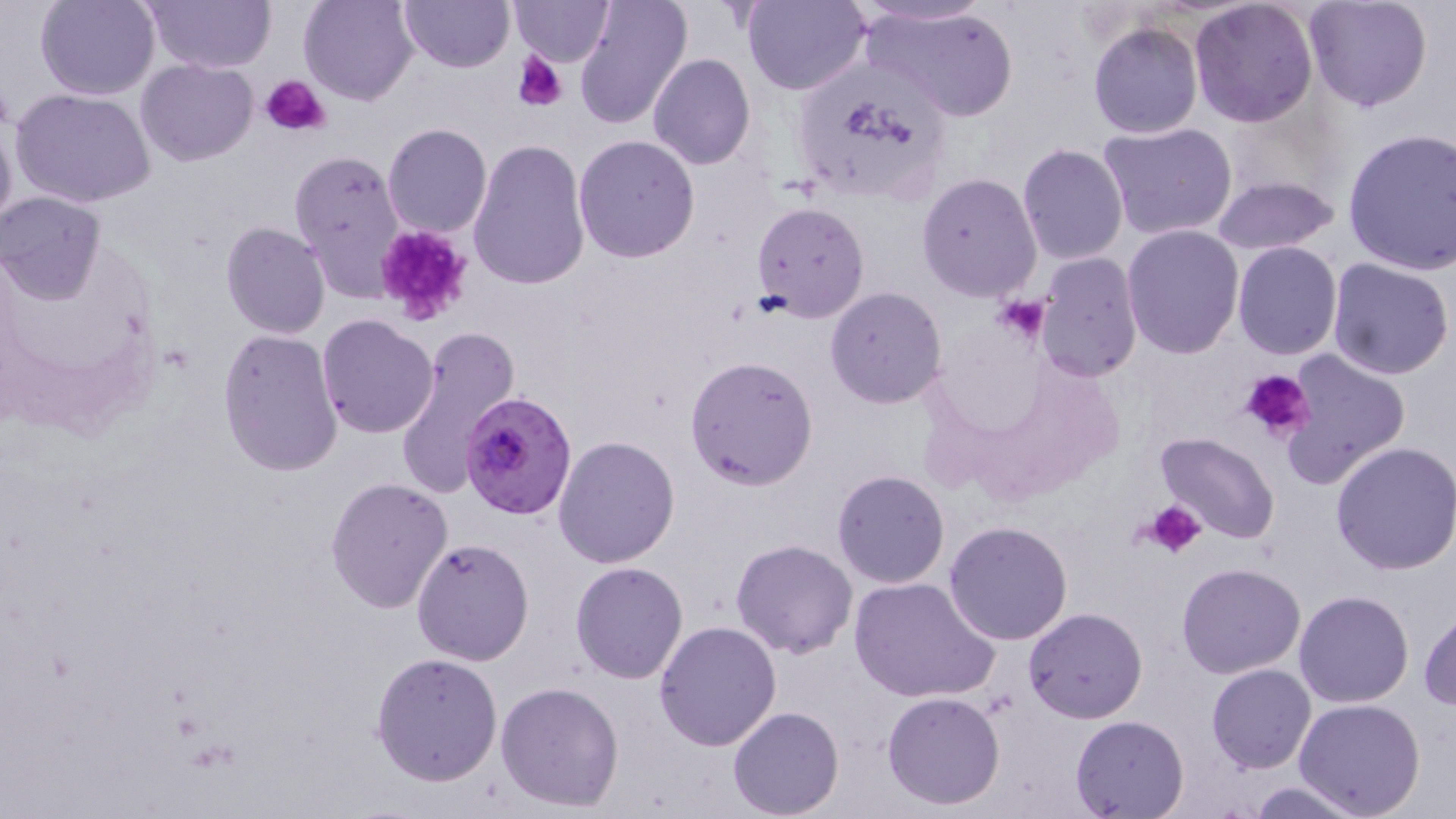 Approximate bounding boxes as named x1/y1/x2/y2 corners in pixels. Uninfected red blood cell locations: (x1=35, y1=0, x2=160, y2=100), (x1=140, y1=0, x2=277, y2=74), (x1=298, y1=0, x2=419, y2=107), (x1=397, y1=0, x2=513, y2=71), (x1=508, y1=0, x2=613, y2=65), (x1=574, y1=0, x2=693, y2=129), (x1=741, y1=0, x2=870, y2=95), (x1=849, y1=0, x2=998, y2=29), (x1=1190, y1=0, x2=1320, y2=128), (x1=1304, y1=0, x2=1434, y2=113), (x1=862, y1=5, x2=1019, y2=122), (x1=1088, y1=22, x2=1202, y2=139), (x1=648, y1=54, x2=756, y2=169), (x1=136, y1=59, x2=257, y2=167), (x1=12, y1=89, x2=155, y2=208), (x1=0, y1=98, x2=18, y2=243), (x1=1098, y1=122, x2=1240, y2=242), (x1=383, y1=123, x2=493, y2=239), (x1=1338, y1=127, x2=1456, y2=275), (x1=573, y1=134, x2=701, y2=263), (x1=468, y1=138, x2=591, y2=293), (x1=1017, y1=142, x2=1129, y2=266), (x1=287, y1=147, x2=408, y2=297), (x1=916, y1=172, x2=1041, y2=303), (x1=1210, y1=177, x2=1341, y2=256), (x1=0, y1=191, x2=107, y2=303), (x1=750, y1=201, x2=870, y2=321), (x1=220, y1=220, x2=332, y2=340), (x1=1121, y1=224, x2=1246, y2=359), (x1=1230, y1=241, x2=1342, y2=361), (x1=1034, y1=252, x2=1143, y2=380), (x1=1328, y1=259, x2=1455, y2=381), (x1=825, y1=286, x2=948, y2=408), (x1=316, y1=314, x2=439, y2=439), (x1=396, y1=323, x2=521, y2=500), (x1=216, y1=327, x2=344, y2=477), (x1=1277, y1=349, x2=1411, y2=488), (x1=685, y1=356, x2=819, y2=490), (x1=1156, y1=433, x2=1281, y2=544), (x1=553, y1=435, x2=681, y2=568), (x1=1330, y1=440, x2=1456, y2=575), (x1=831, y1=470, x2=951, y2=590), (x1=325, y1=477, x2=454, y2=613), (x1=944, y1=522, x2=1075, y2=645), (x1=411, y1=537, x2=534, y2=666), (x1=730, y1=539, x2=859, y2=658), (x1=570, y1=561, x2=689, y2=684), (x1=1176, y1=563, x2=1306, y2=680), (x1=848, y1=576, x2=1000, y2=704), (x1=1294, y1=591, x2=1414, y2=708), (x1=1022, y1=607, x2=1147, y2=724), (x1=1419, y1=609, x2=1456, y2=710), (x1=655, y1=622, x2=783, y2=751), (x1=371, y1=652, x2=503, y2=787), (x1=1206, y1=664, x2=1316, y2=774), (x1=495, y1=680, x2=625, y2=813), (x1=881, y1=692, x2=1006, y2=811), (x1=1294, y1=698, x2=1427, y2=819), (x1=728, y1=707, x2=845, y2=819), (x1=1069, y1=715, x2=1189, y2=818), (x1=1245, y1=780, x2=1365, y2=818). Platelet locations: (x1=516, y1=52, x2=568, y2=110), (x1=259, y1=75, x2=331, y2=138), (x1=372, y1=221, x2=476, y2=324), (x1=994, y1=295, x2=1049, y2=345), (x1=1238, y1=368, x2=1314, y2=444), (x1=1145, y1=500, x2=1208, y2=558). Plasmodium falciparum-infected red blood cell locations: (x1=460, y1=393, x2=575, y2=519). Slide-level diagnosis: Plasmodium falciparum. Captured at 1000x magnification. Thin blood smear. Optical microscopy. May-Grünwald-Giemsa stain. Image is 1456×819 pixels. Single field of view.